Give the extent of all Plasmodium falciparum-infected red blood cells.
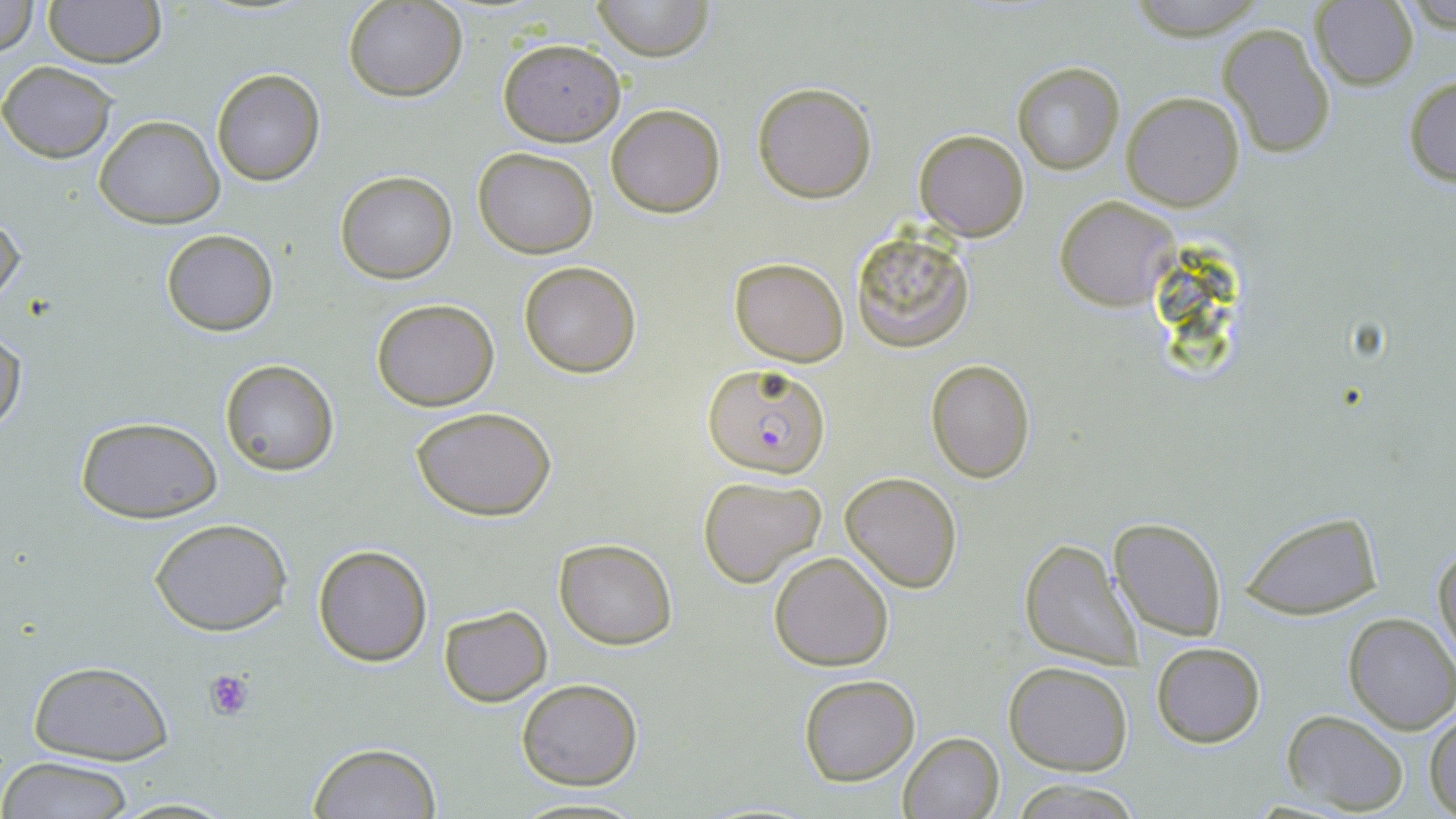

Approximate bounding boxes as (x1, y1, x2, y2) in pixels.
Plasmodium falciparum-infected red blood cells: (703, 364, 830, 478).

Summary:
  - Platelet locations: (202, 668, 255, 721)
  - Uninfected red blood cell locations: (0, 0, 38, 57), (43, 0, 166, 69), (591, 0, 715, 61), (1121, 0, 1269, 36), (345, 1, 466, 101), (1309, 1, 1420, 90), (1216, 23, 1336, 160), (496, 38, 626, 145), (1, 62, 116, 163), (1011, 62, 1124, 174), (209, 67, 326, 186), (1403, 73, 1456, 187), (753, 82, 876, 203), (1121, 93, 1245, 211), (605, 102, 725, 218), (95, 115, 224, 229), (914, 129, 1030, 241), (473, 147, 599, 258), (334, 170, 457, 283), (1054, 195, 1178, 311), (0, 208, 25, 307), (161, 228, 278, 336), (851, 231, 974, 352), (730, 256, 849, 367), (518, 261, 640, 378), (371, 297, 499, 412), (0, 330, 27, 438), (926, 357, 1035, 483), (219, 358, 340, 478), (411, 405, 558, 519), (75, 415, 223, 523), (841, 471, 963, 593), (697, 474, 828, 589), (1237, 510, 1386, 623), (1110, 515, 1228, 641), (150, 518, 292, 636), (553, 538, 677, 650), (1019, 538, 1144, 669), (1433, 540, 1456, 671), (312, 544, 432, 665), (769, 551, 894, 672), (438, 604, 552, 707), (1341, 611, 1456, 734), (1151, 641, 1266, 748), (1004, 659, 1133, 773), (26, 660, 174, 765), (798, 675, 921, 786), (516, 678, 643, 789), (1281, 710, 1408, 814), (1427, 710, 1456, 817), (898, 732, 1004, 819), (306, 742, 442, 818), (0, 757, 139, 818), (103, 795, 243, 817), (507, 795, 647, 818)
  - Slide-level diagnosis: Plasmodium falciparum
  - Stain: May-Grünwald-Giemsa
  - Image size: 1456×819 pixels
  - Modality: optical microscopy
  - Field of view: one of a larger specimen
  - Preparation: thin blood film
  - Magnification: 1000x